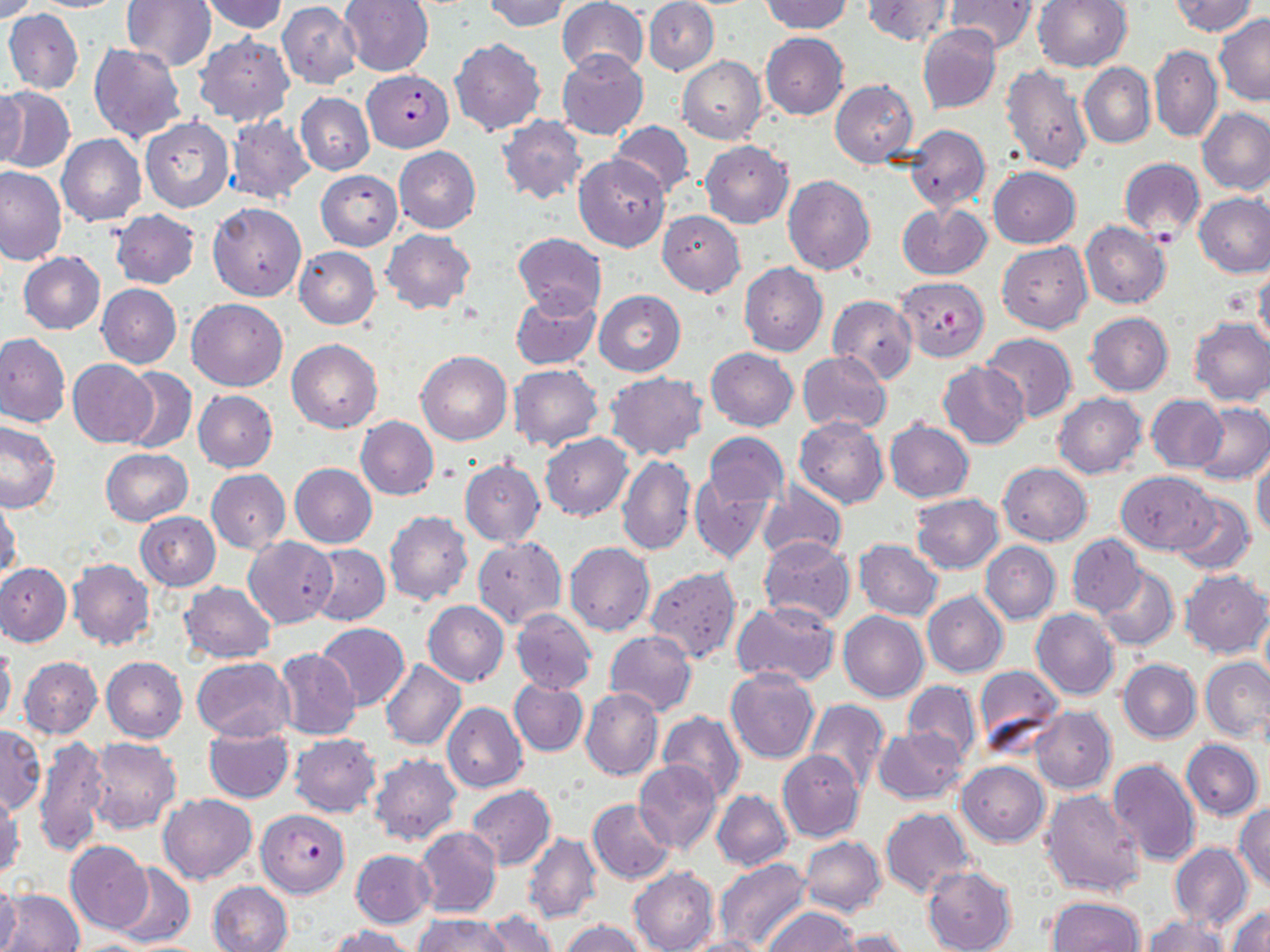
{
  "plasmodium_falciparum_infected_red_blood_cell_locations": "approximate bounding boxes as named x1/y1/x2/y2 corners in pixels: (x1=363, y1=71, x2=454, y2=152), (x1=896, y1=277, x2=990, y2=361), (x1=257, y1=809, x2=350, y2=897)",
  "slide_level_diagnosis": "Plasmodium falciparum",
  "uninfected_red_blood_cell_locations": "approximate bounding boxes as named x1/y1/x2/y2 corners in pixels: (x1=2, y1=0, x2=39, y2=23), (x1=122, y1=0, x2=217, y2=71), (x1=340, y1=0, x2=433, y2=76), (x1=482, y1=0, x2=570, y2=32), (x1=558, y1=0, x2=650, y2=78), (x1=760, y1=0, x2=852, y2=34), (x1=863, y1=0, x2=953, y2=46), (x1=1033, y1=0, x2=1132, y2=72), (x1=1169, y1=0, x2=1259, y2=36), (x1=25, y1=1, x2=128, y2=12), (x1=198, y1=1, x2=287, y2=34), (x1=644, y1=1, x2=718, y2=75), (x1=946, y1=1, x2=1036, y2=54), (x1=277, y1=3, x2=362, y2=89), (x1=4, y1=8, x2=83, y2=95), (x1=1213, y1=14, x2=1270, y2=106), (x1=917, y1=24, x2=1001, y2=113), (x1=761, y1=32, x2=849, y2=120), (x1=194, y1=33, x2=294, y2=128), (x1=450, y1=37, x2=545, y2=136), (x1=88, y1=41, x2=186, y2=143), (x1=1149, y1=44, x2=1221, y2=142), (x1=558, y1=49, x2=650, y2=139), (x1=678, y1=56, x2=766, y2=145), (x1=999, y1=60, x2=1092, y2=175), (x1=1079, y1=62, x2=1155, y2=149), (x1=831, y1=79, x2=920, y2=169), (x1=0, y1=87, x2=75, y2=174), (x1=0, y1=88, x2=28, y2=173), (x1=296, y1=92, x2=375, y2=174), (x1=1196, y1=108, x2=1270, y2=196), (x1=225, y1=114, x2=315, y2=203), (x1=496, y1=115, x2=587, y2=205), (x1=140, y1=116, x2=234, y2=213), (x1=609, y1=120, x2=695, y2=197), (x1=907, y1=123, x2=990, y2=211), (x1=57, y1=135, x2=146, y2=225), (x1=699, y1=141, x2=794, y2=228), (x1=394, y1=145, x2=481, y2=233), (x1=575, y1=154, x2=670, y2=252), (x1=1119, y1=158, x2=1205, y2=240), (x1=0, y1=165, x2=66, y2=264), (x1=988, y1=166, x2=1080, y2=248), (x1=316, y1=170, x2=402, y2=251), (x1=783, y1=176, x2=875, y2=277), (x1=1194, y1=193, x2=1270, y2=277), (x1=208, y1=202, x2=307, y2=302), (x1=897, y1=202, x2=991, y2=280), (x1=110, y1=209, x2=200, y2=289), (x1=106, y1=210, x2=189, y2=367), (x1=656, y1=211, x2=745, y2=297), (x1=1080, y1=220, x2=1171, y2=308), (x1=381, y1=228, x2=475, y2=314), (x1=513, y1=232, x2=606, y2=317), (x1=997, y1=243, x2=1092, y2=333), (x1=294, y1=247, x2=380, y2=329), (x1=18, y1=252, x2=105, y2=334), (x1=739, y1=262, x2=828, y2=357), (x1=1254, y1=264, x2=1270, y2=351), (x1=96, y1=284, x2=181, y2=368), (x1=510, y1=289, x2=601, y2=371), (x1=594, y1=290, x2=685, y2=376), (x1=828, y1=294, x2=917, y2=385), (x1=186, y1=299, x2=288, y2=391), (x1=1085, y1=312, x2=1173, y2=395), (x1=1189, y1=317, x2=1270, y2=406), (x1=0, y1=332, x2=70, y2=427), (x1=980, y1=333, x2=1077, y2=422), (x1=287, y1=338, x2=383, y2=432), (x1=705, y1=348, x2=798, y2=431), (x1=417, y1=350, x2=512, y2=446), (x1=798, y1=351, x2=892, y2=434), (x1=68, y1=360, x2=159, y2=447), (x1=938, y1=361, x2=1029, y2=449), (x1=508, y1=364, x2=604, y2=451), (x1=119, y1=366, x2=196, y2=454), (x1=606, y1=373, x2=709, y2=461), (x1=193, y1=390, x2=278, y2=472), (x1=1052, y1=393, x2=1146, y2=479), (x1=1148, y1=395, x2=1227, y2=473), (x1=1194, y1=403, x2=1270, y2=483), (x1=355, y1=415, x2=438, y2=501), (x1=795, y1=417, x2=888, y2=508), (x1=885, y1=418, x2=973, y2=502), (x1=0, y1=420, x2=61, y2=512), (x1=540, y1=432, x2=633, y2=520), (x1=704, y1=433, x2=788, y2=510), (x1=543, y1=446, x2=692, y2=544), (x1=101, y1=448, x2=193, y2=526), (x1=617, y1=455, x2=696, y2=555), (x1=1252, y1=456, x2=1270, y2=537), (x1=460, y1=459, x2=545, y2=548), (x1=998, y1=462, x2=1092, y2=546), (x1=290, y1=463, x2=378, y2=548), (x1=207, y1=469, x2=290, y2=553), (x1=689, y1=471, x2=773, y2=563), (x1=1117, y1=471, x2=1216, y2=553), (x1=757, y1=481, x2=846, y2=564), (x1=1170, y1=493, x2=1256, y2=576), (x1=911, y1=494, x2=1004, y2=574), (x1=1, y1=496, x2=22, y2=580), (x1=385, y1=510, x2=473, y2=605), (x1=136, y1=512, x2=221, y2=590), (x1=1067, y1=534, x2=1145, y2=617), (x1=473, y1=536, x2=566, y2=628), (x1=244, y1=537, x2=337, y2=628), (x1=758, y1=538, x2=854, y2=625), (x1=854, y1=539, x2=942, y2=619), (x1=981, y1=542, x2=1060, y2=624), (x1=565, y1=543, x2=654, y2=636), (x1=307, y1=544, x2=390, y2=626), (x1=68, y1=558, x2=155, y2=650), (x1=0, y1=563, x2=71, y2=648), (x1=1094, y1=566, x2=1180, y2=650), (x1=646, y1=567, x2=742, y2=662), (x1=1180, y1=570, x2=1269, y2=659), (x1=1194, y1=574, x2=1267, y2=741), (x1=181, y1=582, x2=276, y2=663), (x1=922, y1=591, x2=1008, y2=677), (x1=423, y1=600, x2=509, y2=686), (x1=732, y1=600, x2=840, y2=687), (x1=511, y1=609, x2=596, y2=693), (x1=1031, y1=609, x2=1120, y2=701), (x1=1259, y1=610, x2=1269, y2=693), (x1=838, y1=611, x2=929, y2=702), (x1=315, y1=622, x2=409, y2=710), (x1=605, y1=630, x2=697, y2=715), (x1=0, y1=643, x2=16, y2=728), (x1=275, y1=648, x2=362, y2=740), (x1=19, y1=656, x2=101, y2=739), (x1=101, y1=656, x2=188, y2=742), (x1=192, y1=657, x2=293, y2=740), (x1=380, y1=659, x2=466, y2=751), (x1=1119, y1=659, x2=1200, y2=742), (x1=1202, y1=659, x2=1270, y2=743), (x1=973, y1=665, x2=1064, y2=755), (x1=726, y1=669, x2=819, y2=764), (x1=509, y1=680, x2=588, y2=755), (x1=901, y1=680, x2=983, y2=765), (x1=580, y1=687, x2=663, y2=781), (x1=806, y1=699, x2=889, y2=791), (x1=442, y1=702, x2=527, y2=794), (x1=1030, y1=707, x2=1116, y2=793), (x1=657, y1=711, x2=746, y2=802), (x1=0, y1=724, x2=44, y2=814), (x1=204, y1=726, x2=294, y2=803), (x1=874, y1=727, x2=968, y2=804), (x1=290, y1=734, x2=381, y2=817), (x1=35, y1=736, x2=110, y2=858), (x1=87, y1=736, x2=181, y2=833), (x1=1181, y1=739, x2=1263, y2=820), (x1=778, y1=750, x2=864, y2=843), (x1=369, y1=754, x2=462, y2=845), (x1=633, y1=759, x2=722, y2=854), (x1=1107, y1=759, x2=1201, y2=867), (x1=958, y1=762, x2=1049, y2=846), (x1=467, y1=785, x2=555, y2=870), (x1=712, y1=790, x2=792, y2=871), (x1=1040, y1=790, x2=1147, y2=897), (x1=1, y1=791, x2=24, y2=881), (x1=158, y1=793, x2=256, y2=884), (x1=589, y1=799, x2=675, y2=884), (x1=1234, y1=802, x2=1270, y2=891), (x1=880, y1=807, x2=974, y2=896), (x1=414, y1=826, x2=501, y2=918), (x1=524, y1=832, x2=602, y2=924), (x1=801, y1=836, x2=886, y2=915), (x1=65, y1=842, x2=155, y2=933), (x1=1170, y1=843, x2=1252, y2=929), (x1=351, y1=849, x2=435, y2=928), (x1=714, y1=859, x2=812, y2=949), (x1=112, y1=863, x2=196, y2=948), (x1=923, y1=866, x2=1017, y2=952), (x1=629, y1=867, x2=718, y2=952), (x1=0, y1=880, x2=22, y2=952), (x1=207, y1=881, x2=293, y2=952), (x1=0, y1=887, x2=85, y2=952), (x1=1045, y1=896, x2=1143, y2=952), (x1=1228, y1=905, x2=1270, y2=952), (x1=764, y1=907, x2=858, y2=952), (x1=481, y1=911, x2=558, y2=952), (x1=415, y1=913, x2=509, y2=952), (x1=1143, y1=915, x2=1227, y2=952), (x1=560, y1=920, x2=646, y2=952), (x1=330, y1=924, x2=415, y2=952), (x1=833, y1=929, x2=914, y2=952), (x1=676, y1=936, x2=771, y2=952)",
  "preparation": "thin blood film",
  "field_of_view": "single",
  "image_size": "1270×952 pixels",
  "magnification": "1000x",
  "stain": "May-Grünwald-Giemsa",
  "modality": "optical microscopy"
}